Assess this cell for malaria.
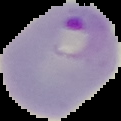
It is parasitized.

image type = segmented cell region on a black background
image size = 121×121 pixels
preparation = thin blood film